Outline each Plasmodium falciparum-infected red blood cell.
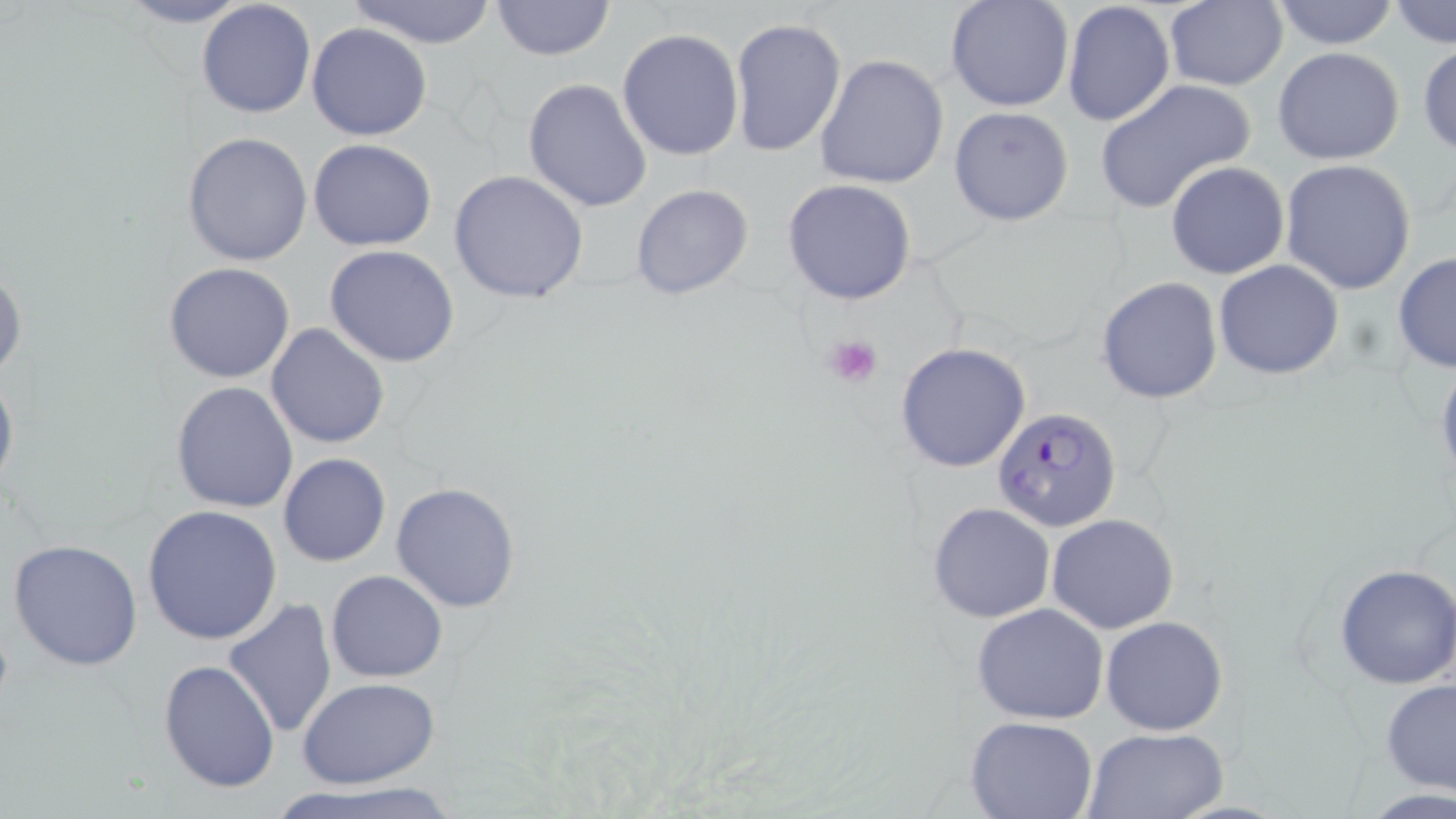
Approximate bounding boxes as named x1/y1/x2/y2 corners in pixels.
Plasmodium falciparum-infected red blood cells: (x1=992, y1=407, x2=1123, y2=534).

Uninfected red blood cell locations: (x1=113, y1=0, x2=258, y2=28), (x1=196, y1=0, x2=317, y2=119), (x1=488, y1=0, x2=616, y2=61), (x1=944, y1=0, x2=1074, y2=111), (x1=348, y1=1, x2=501, y2=47), (x1=1062, y1=1, x2=1176, y2=129), (x1=1161, y1=1, x2=1288, y2=90), (x1=1267, y1=1, x2=1401, y2=50), (x1=1388, y1=1, x2=1454, y2=48), (x1=729, y1=17, x2=846, y2=156), (x1=306, y1=21, x2=433, y2=140), (x1=616, y1=30, x2=744, y2=160), (x1=1417, y1=42, x2=1456, y2=158), (x1=1272, y1=47, x2=1406, y2=164), (x1=815, y1=55, x2=951, y2=190), (x1=523, y1=78, x2=654, y2=215), (x1=1094, y1=79, x2=1256, y2=214), (x1=949, y1=106, x2=1075, y2=226), (x1=181, y1=131, x2=315, y2=267), (x1=309, y1=139, x2=437, y2=252), (x1=1279, y1=159, x2=1417, y2=295), (x1=1165, y1=160, x2=1289, y2=279), (x1=448, y1=169, x2=589, y2=305), (x1=782, y1=179, x2=916, y2=303), (x1=630, y1=183, x2=754, y2=301), (x1=325, y1=244, x2=459, y2=368), (x1=1392, y1=251, x2=1456, y2=376), (x1=1213, y1=259, x2=1344, y2=381), (x1=0, y1=261, x2=26, y2=384), (x1=163, y1=262, x2=296, y2=383), (x1=1096, y1=276, x2=1223, y2=405), (x1=265, y1=323, x2=390, y2=450), (x1=894, y1=342, x2=1031, y2=472), (x1=1434, y1=356, x2=1456, y2=490), (x1=0, y1=364, x2=18, y2=498), (x1=171, y1=381, x2=298, y2=513), (x1=278, y1=453, x2=391, y2=567), (x1=392, y1=482, x2=523, y2=613), (x1=927, y1=502, x2=1056, y2=623), (x1=142, y1=506, x2=283, y2=647), (x1=1047, y1=513, x2=1180, y2=635), (x1=8, y1=537, x2=143, y2=672), (x1=1333, y1=562, x2=1456, y2=688), (x1=325, y1=570, x2=447, y2=682), (x1=222, y1=599, x2=338, y2=739), (x1=971, y1=602, x2=1109, y2=724), (x1=1100, y1=616, x2=1228, y2=736), (x1=158, y1=659, x2=280, y2=795), (x1=298, y1=677, x2=441, y2=789), (x1=1380, y1=679, x2=1456, y2=796), (x1=965, y1=716, x2=1097, y2=819), (x1=1080, y1=727, x2=1231, y2=819), (x1=273, y1=781, x2=466, y2=819). Platelet locations: (x1=823, y1=333, x2=884, y2=388). Slide-level diagnosis: Plasmodium falciparum. One field of a larger specimen. Image is 1456×819 pixels. 1000x magnification. Thin blood smear. May-Grünwald-Giemsa-stained preparation. Optical microscopy.